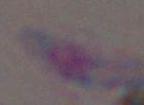
magnification: 1000x
identification: Toxoplasma gondii
modality: photomicrograph